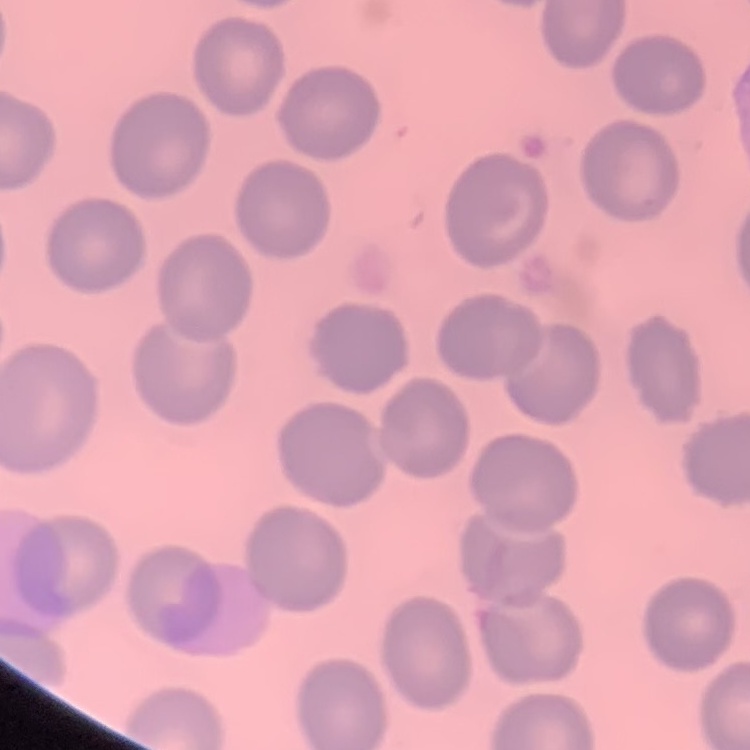
Summary:
  - Red blood cell morphology: no rouleaux formation
  - Image type: square crop of a larger photomicrograph
  - Stain: Field's or Giemsa
  - Preparation: thin blood film